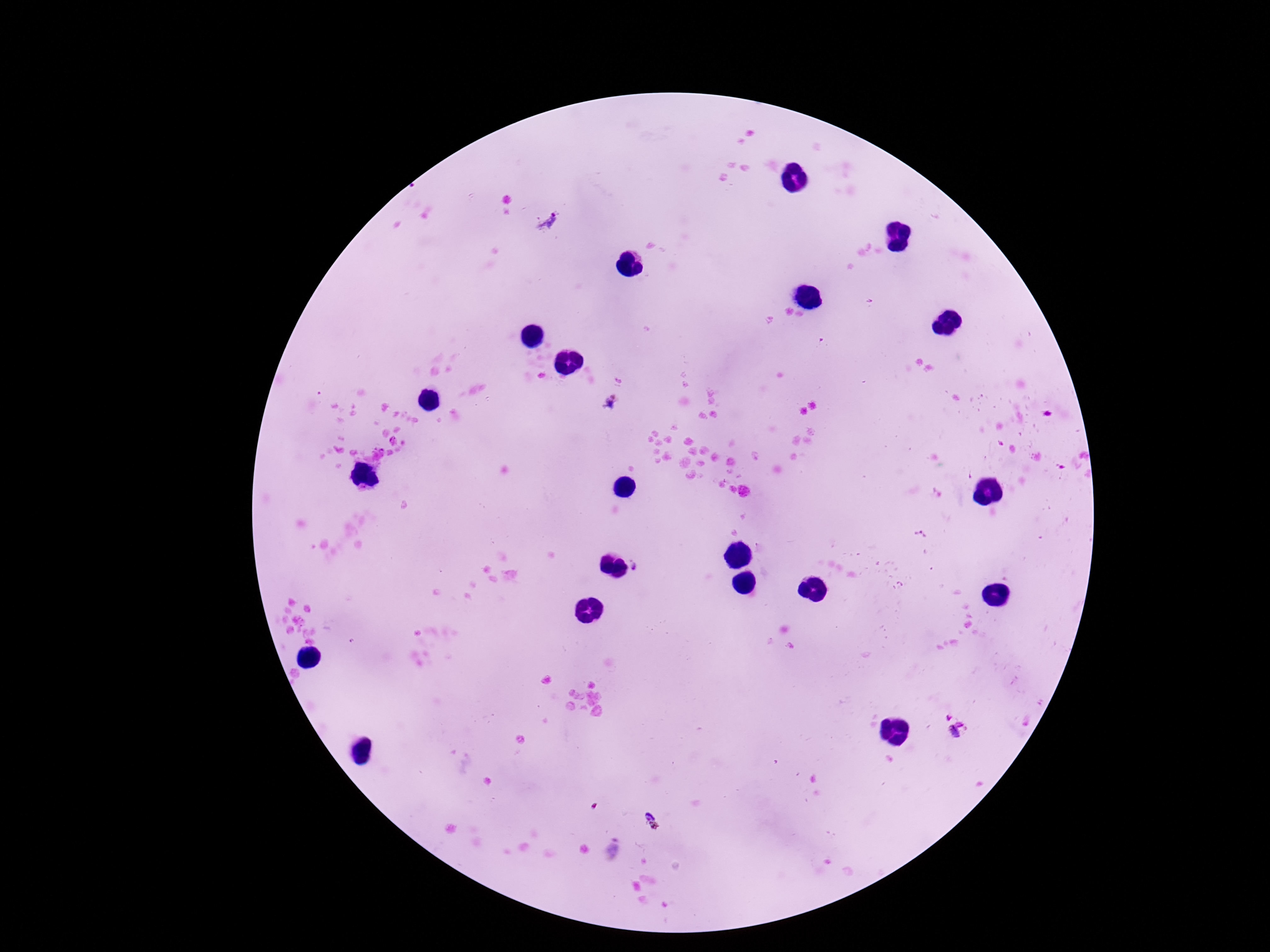
{
  "image_size": "1270×952 pixels",
  "plasmodium_parasite_locations": "approximate centers as [x, y] in pixels: [549, 223], [612, 405], [920, 535], [637, 568], [954, 735], [652, 821], [613, 850]",
  "field_of_view": "single",
  "capture": "smartphone camera through the microscope eyepiece",
  "patient_malaria_status": "infected",
  "preparation": "thick peripheral-blood smear",
  "stain": "Giemsa",
  "magnification": "100x"
}